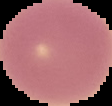

{
  "image_type": "segmented cell region with the area outside set to black",
  "preparation": "thin blood film",
  "malaria_status": "uninfected",
  "image_size": "112×106 pixels"
}